Identify the blood parasite species.
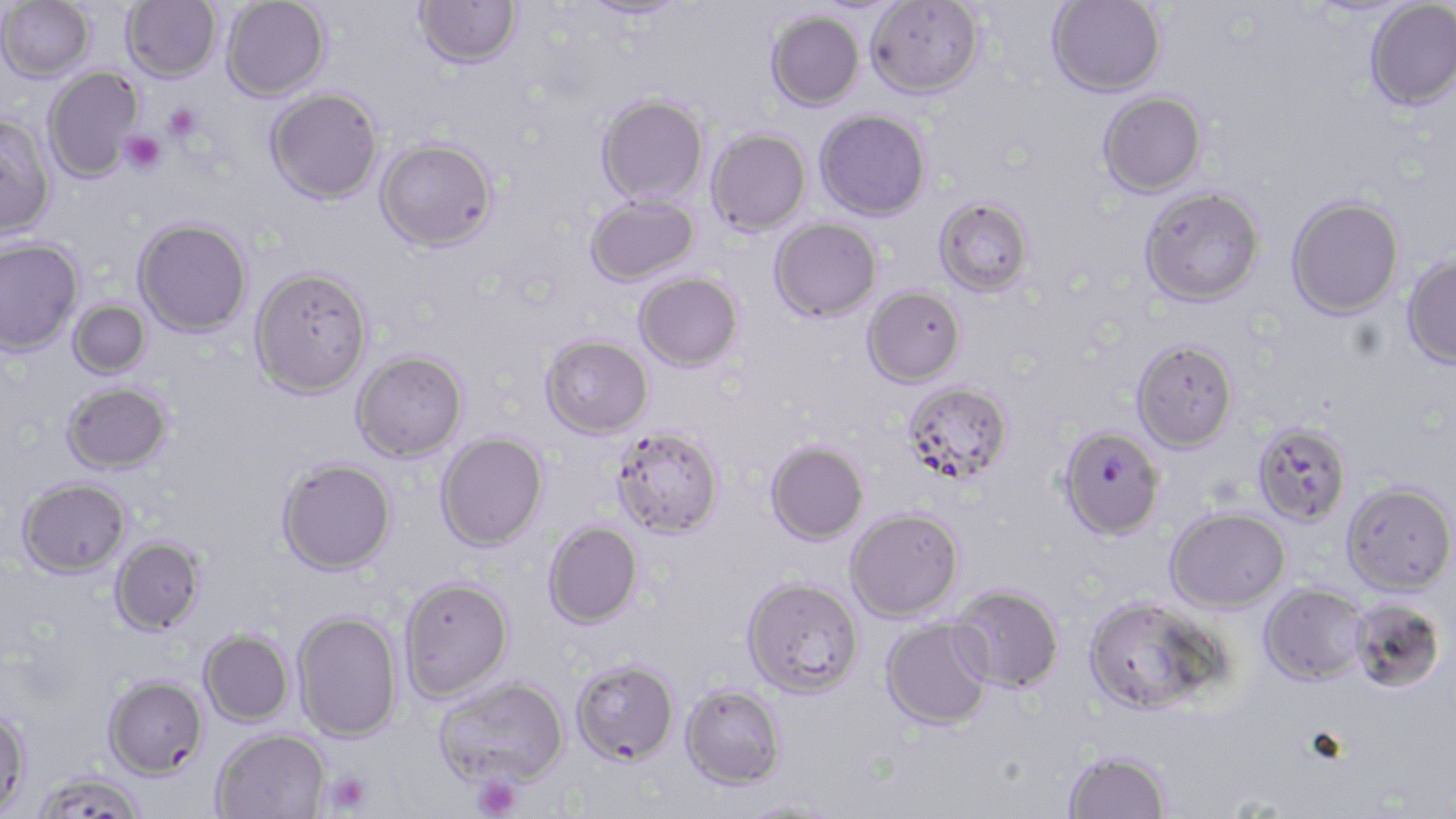

Plasmodium falciparum.

stain: May-Grünwald-Giemsa
preparation: thin blood film
uninfected_red_blood_cell_locations: 'approximate bounding boxes as (x1, y1, x2, y2) in pixels: (121, 0, 221, 82), (221, 0, 330, 101), (414, 0, 522, 69), (581, 0, 688, 20), (866, 0, 984, 98), (1047, 0, 1165, 97), (0, 1, 95, 83), (1364, 1, 1456, 112), (767, 11, 865, 110), (43, 67, 143, 181), (265, 88, 383, 204), (1098, 91, 1207, 197), (597, 94, 708, 205), (815, 109, 931, 221), (0, 115, 55, 240), (706, 129, 811, 236), (376, 138, 497, 252), (1139, 186, 1265, 307), (586, 194, 699, 287), (1286, 196, 1404, 319), (934, 198, 1033, 297), (133, 217, 252, 337), (770, 218, 881, 322), (0, 239, 83, 356), (1402, 251, 1456, 370), (250, 267, 373, 398), (634, 272, 743, 371), (862, 286, 966, 387), (68, 299, 152, 379), (540, 334, 653, 438), (1131, 339, 1238, 452), (352, 350, 468, 463), (62, 381, 173, 473), (903, 382, 1013, 483), (1252, 422, 1351, 526), (611, 427, 724, 539), (436, 431, 548, 552), (766, 440, 868, 544), (276, 457, 397, 575), (17, 476, 131, 579), (1341, 481, 1455, 595), (845, 507, 964, 622), (1166, 507, 1291, 613), (543, 521, 643, 628), (109, 535, 206, 635), (399, 576, 514, 704), (742, 576, 864, 698), (1259, 583, 1368, 686), (950, 584, 1064, 693), (1083, 596, 1225, 715), (1350, 597, 1447, 694), (292, 610, 402, 742), (880, 617, 994, 731), (198, 629, 294, 727), (571, 658, 679, 765), (103, 674, 207, 778), (435, 676, 570, 789), (680, 684, 786, 789), (0, 705, 30, 817), (212, 728, 330, 819), (1063, 749, 1172, 818), (30, 771, 148, 818), (737, 799, 843, 818)'
magnification: 1000x
plasmodium_falciparum_infected_red_blood_cell_locations: 'approximate bounding boxes as (x1, y1, x2, y2) in pixels: (1059, 426, 1165, 540)'
image_size: 1456×819 pixels
platelet_locations: 'approximate bounding boxes as (x1, y1, x2, y2) in pixels: (163, 102, 202, 142), (121, 130, 166, 175), (323, 769, 374, 816), (472, 774, 523, 819)'
field_of_view: one of a larger specimen
modality: light microscopy